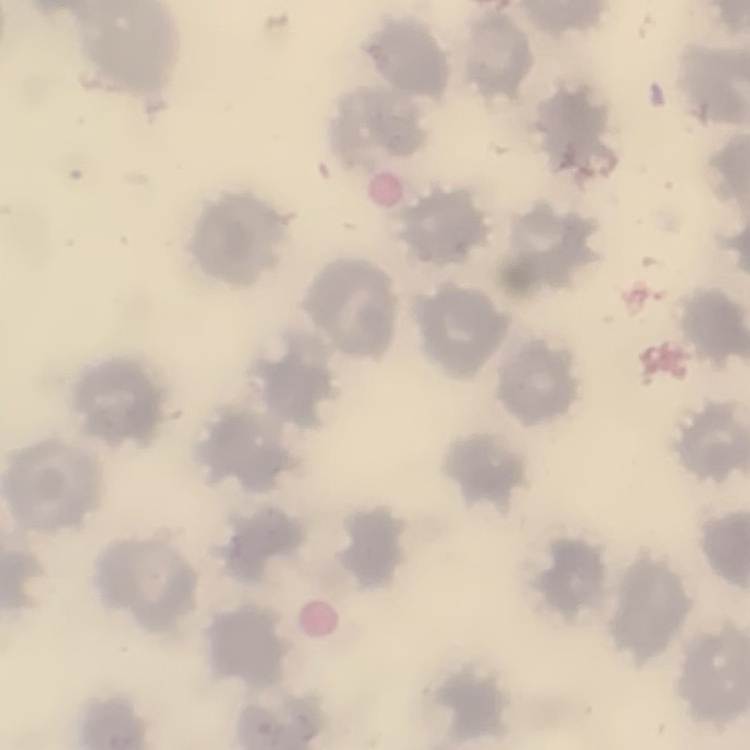
Summary:
  - Erythrocyte morphology: no rouleaux formation
  - Preparation: thin peripheral smear
  - Image type: square crop of a larger photomicrograph
  - Stain: Field's or Giemsa